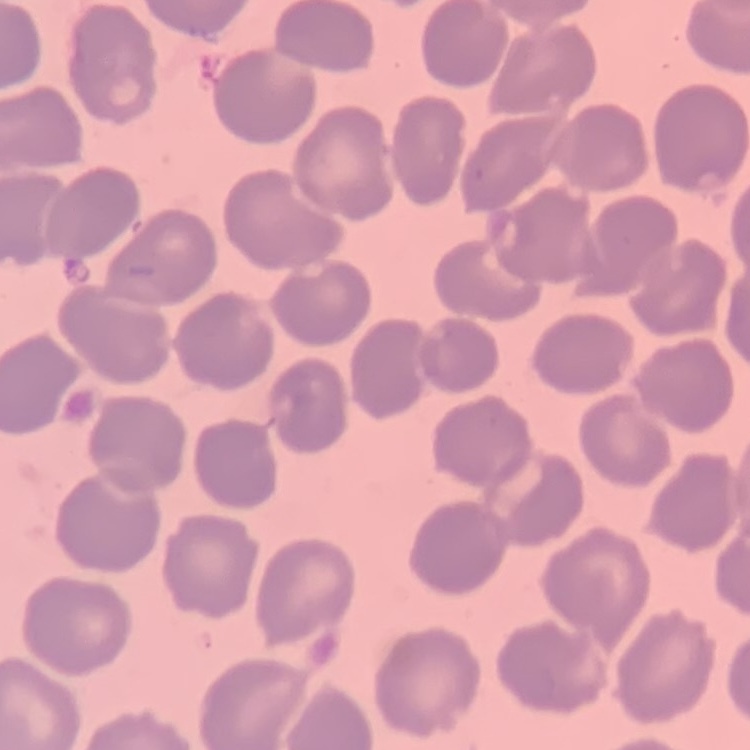
The erythrocytes exhibit no rouleaux formation. Thin peripheral smear. Field's or Giemsa stain. Square crop of a larger photomicrograph.